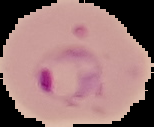

preparation = thin blood film
image size = 154×127 pixels
image type = segmented cell region with the area outside set to black
malaria status = parasitized